Assess this cell for malaria.
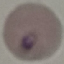

Parasitized.

capture: smartphone through the microscope eyepiece
preparation: thin smear
stain: Giemsa
image_type: automatically extracted cell patch, resized to 64 × 64 pixels